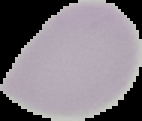 Malaria status: uninfected. The area outside the segmented cell region is set to black. Image is 142×121 pixels. From a thin blood film.